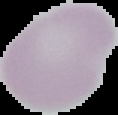

Summary:
  - Image type: cell region segmented out of the field of view; surrounding area masked to black
  - Result: no malaria parasites seen
  - Image size: 118×115 pixels
  - Preparation: thin blood smear